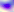
{
  "identification": "Toxoplasma gondii",
  "magnification": "400x",
  "modality": "micrograph"
}